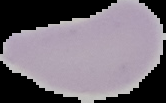
image size = 166×103 pixels
image type = segmented cell region with the area outside set to black
preparation = thin blood film
malaria status = uninfected